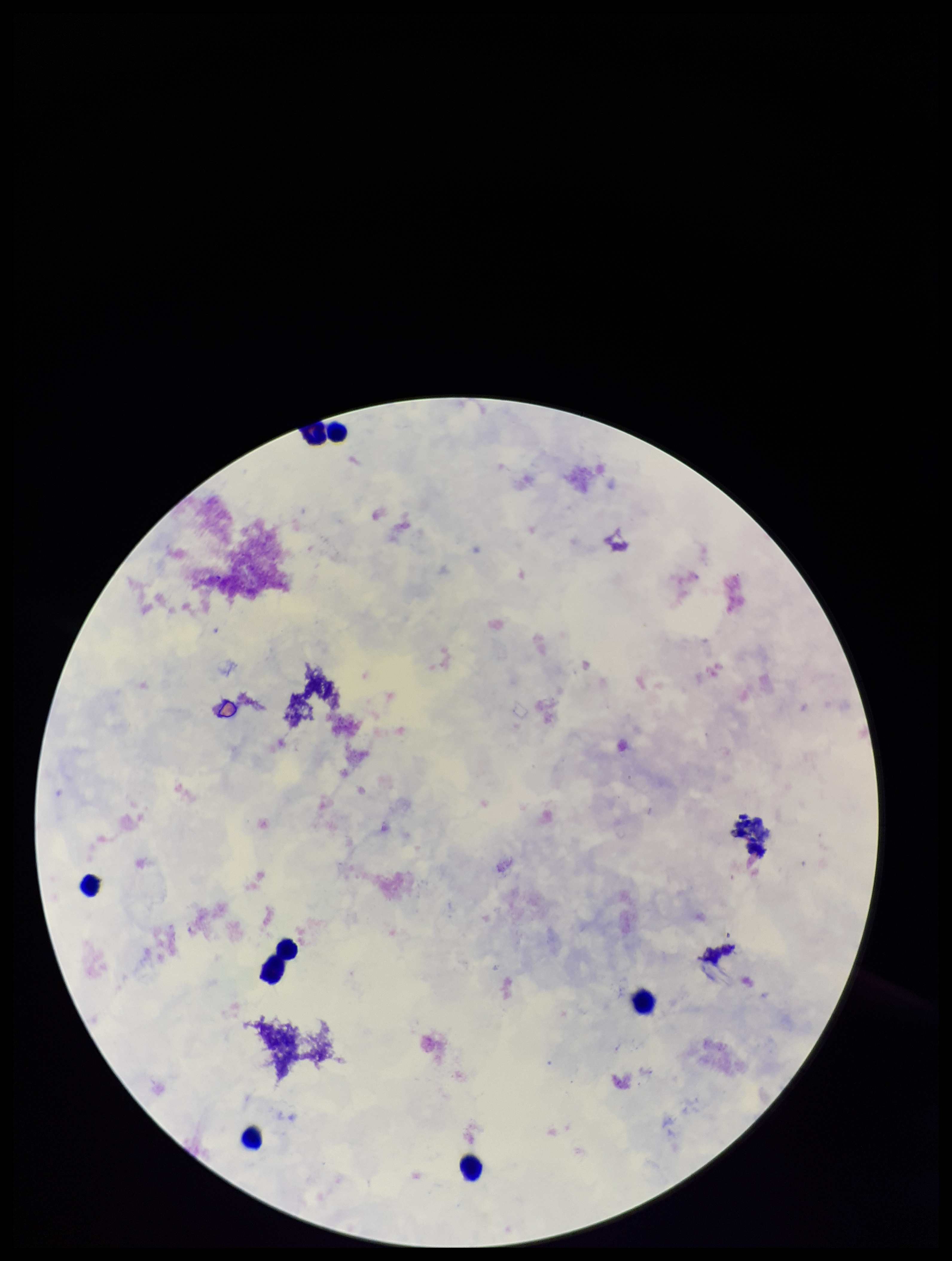

Summary:
  - Image size: 952×1261 pixels
  - Leukocyte count: 6
  - Capture: smartphone photograph through the microscope eyepiece
  - Plasmodium parasites: none identified
  - Stain: Giemsa
  - Parasite count: 0
  - Preparation: thick smear
  - Field of view: one from this slide
  - Patient malaria status: negative